Give the position of every malaria parasite.
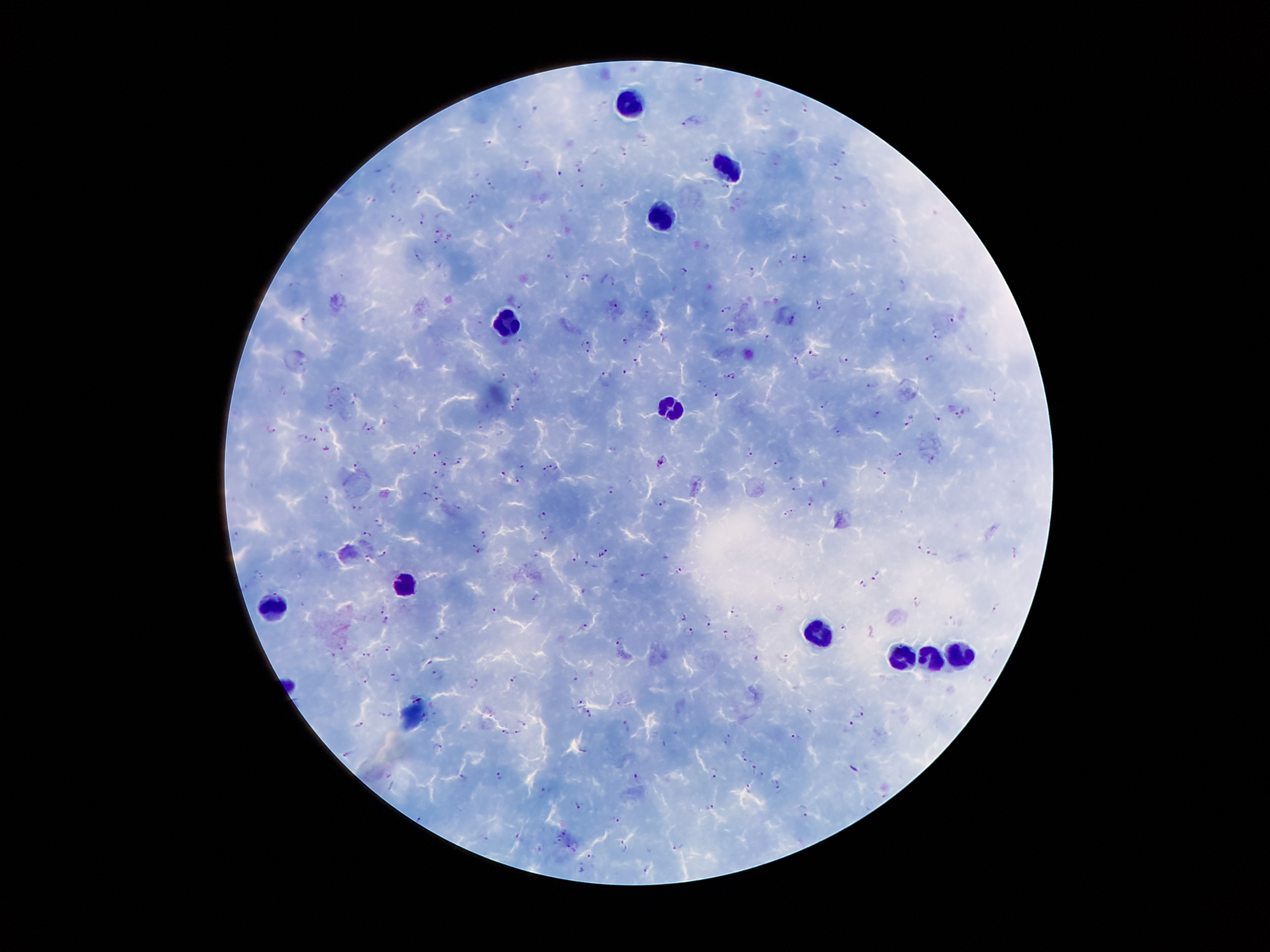
Approximate object centers, in pixels from the top-left corner.
Malaria parasites: (x=806, y=107), (x=767, y=108), (x=688, y=122), (x=488, y=144), (x=624, y=151), (x=704, y=159), (x=836, y=162), (x=527, y=164), (x=580, y=166), (x=560, y=172), (x=489, y=181), (x=582, y=183), (x=393, y=188), (x=725, y=188), (x=473, y=198), (x=396, y=218), (x=423, y=219), (x=439, y=232), (x=436, y=243), (x=417, y=255), (x=552, y=255), (x=806, y=255), (x=794, y=256), (x=684, y=271), (x=752, y=271), (x=567, y=276), (x=585, y=276), (x=818, y=304), (x=611, y=305), (x=520, y=307), (x=889, y=307), (x=726, y=310), (x=648, y=313), (x=793, y=315), (x=951, y=316), (x=304, y=318), (x=729, y=330), (x=938, y=335), (x=768, y=337), (x=521, y=340), (x=625, y=342), (x=588, y=345), (x=814, y=353), (x=844, y=358), (x=635, y=359), (x=794, y=360), (x=930, y=360), (x=626, y=372), (x=606, y=375), (x=734, y=375), (x=727, y=376), (x=503, y=377), (x=872, y=385), (x=283, y=389), (x=337, y=390), (x=716, y=393), (x=993, y=393), (x=517, y=399), (x=825, y=404), (x=332, y=407), (x=875, y=414), (x=959, y=415), (x=941, y=419), (x=908, y=422), (x=479, y=423), (x=270, y=429), (x=372, y=429), (x=324, y=430), (x=837, y=433), (x=302, y=437), (x=313, y=440), (x=416, y=451), (x=437, y=452), (x=749, y=453), (x=898, y=453), (x=932, y=458), (x=779, y=461), (x=458, y=462), (x=358, y=463), (x=443, y=463), (x=660, y=463), (x=522, y=466), (x=553, y=466), (x=545, y=470), (x=881, y=471), (x=503, y=474), (x=439, y=476), (x=793, y=478), (x=518, y=479), (x=438, y=488), (x=610, y=488), (x=795, y=489), (x=429, y=495), (x=326, y=498), (x=439, y=499), (x=660, y=502), (x=358, y=508), (x=458, y=509), (x=793, y=511), (x=785, y=512), (x=541, y=515), (x=379, y=521), (x=236, y=534), (x=484, y=535), (x=545, y=535), (x=367, y=536), (x=922, y=543), (x=476, y=550), (x=606, y=550), (x=932, y=552), (x=382, y=554), (x=600, y=554), (x=536, y=555), (x=576, y=559), (x=368, y=560), (x=591, y=565), (x=680, y=571), (x=259, y=574), (x=645, y=575), (x=876, y=575), (x=246, y=585), (x=864, y=586), (x=583, y=590), (x=535, y=599), (x=917, y=601), (x=995, y=608), (x=382, y=609), (x=733, y=609), (x=495, y=611), (x=684, y=614), (x=709, y=618), (x=386, y=619), (x=953, y=620), (x=583, y=627), (x=843, y=628), (x=690, y=633), (x=727, y=634), (x=438, y=637), (x=619, y=641), (x=339, y=647), (x=387, y=648), (x=997, y=652), (x=331, y=654), (x=367, y=654), (x=757, y=658), (x=784, y=658), (x=430, y=661), (x=437, y=674), (x=395, y=676), (x=576, y=676), (x=366, y=678), (x=514, y=679), (x=988, y=679), (x=476, y=681), (x=577, y=702), (x=589, y=711), (x=857, y=712), (x=386, y=714), (x=523, y=724), (x=851, y=725), (x=359, y=726), (x=625, y=726), (x=505, y=732), (x=517, y=732), (x=797, y=737), (x=728, y=738), (x=437, y=744), (x=584, y=748), (x=349, y=752), (x=744, y=759), (x=854, y=768), (x=753, y=770), (x=499, y=772), (x=714, y=772), (x=762, y=775), (x=463, y=777), (x=638, y=778), (x=749, y=787), (x=776, y=789), (x=548, y=792), (x=579, y=804), (x=710, y=807), (x=804, y=810), (x=420, y=819), (x=615, y=819), (x=565, y=832), (x=519, y=837), (x=558, y=839), (x=569, y=843), (x=624, y=846), (x=677, y=846), (x=576, y=851), (x=592, y=856), (x=647, y=869), (x=582, y=871).

Leukocyte locations: (x=624, y=103), (x=724, y=170), (x=659, y=218), (x=506, y=328), (x=670, y=408), (x=399, y=586), (x=275, y=607), (x=816, y=634), (x=955, y=655), (x=901, y=657), (x=929, y=662). Single field of view. Patient malaria status: infected with Plasmodium falciparum. 100x magnification. Image is 1270×952 pixels. Giemsa stain. Smartphone photograph taken through the microscope eyepiece. Thick blood film.